Report the malaria status of this cell.
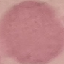
It is uninfected.

Summary:
  - Preparation: thin smear
  - Capture: smartphone through the microscope eyepiece
  - Image type: automatically extracted cell patch, resized to 64 × 64 pixels
  - Stain: Giemsa